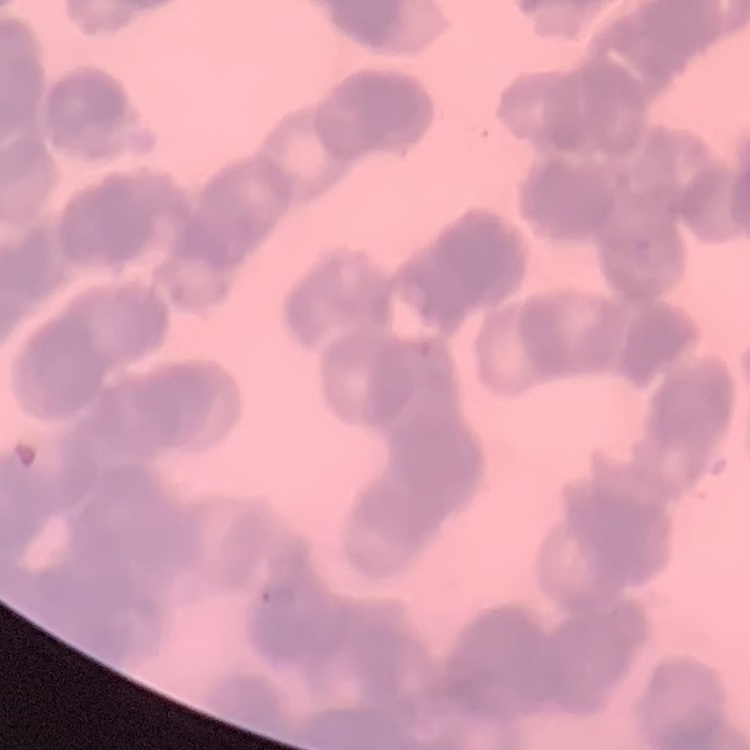
erythrocyte morphology = rouleaux formation
image type = one tile cut from a larger photomicrograph
preparation = thin peripheral smear
stain = Field's or Giemsa